Report the malaria status of this cell.
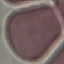

It is uninfected.

Summary:
  - Image type: automatically extracted cell patch, resized to 64 × 64 pixels
  - Capture: smartphone through the microscope eyepiece
  - Preparation: thin smear
  - Stain: Giemsa